Identify the parasite.
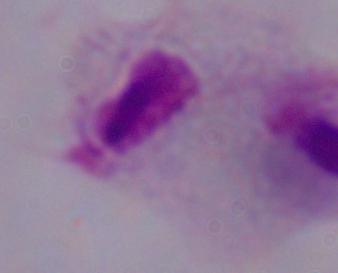

This is a trichomonad.

magnification = 1000x
modality = micrograph